Classify this cell by malaria status.
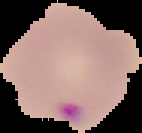

Parasitized.

From a thin blood smear. Cell region segmented out of the field of view; the surrounding area is masked to black. Image is 142×133 pixels.